Report the malaria status of this cell.
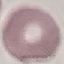

Uninfected.

{
  "image_type": "cell patch, automatically extracted from a larger field of view and resized to 64 × 64 pixels",
  "stain": "Giemsa",
  "capture": "smartphone through the microscope eyepiece",
  "preparation": "thin blood smear"
}